Identify the parasite.
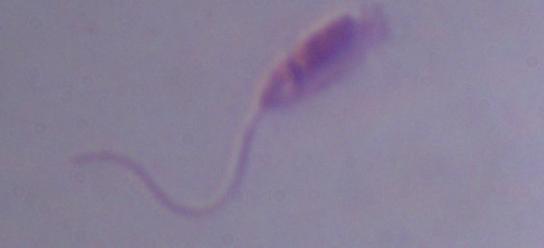

Leishmania.

1000x magnification. Photomicrograph.